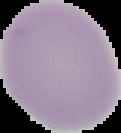

image type = cell region segmented out of the field of view; surrounding area masked to black
image size = 121×133 pixels
preparation = thin blood film
result = negative for malaria parasites